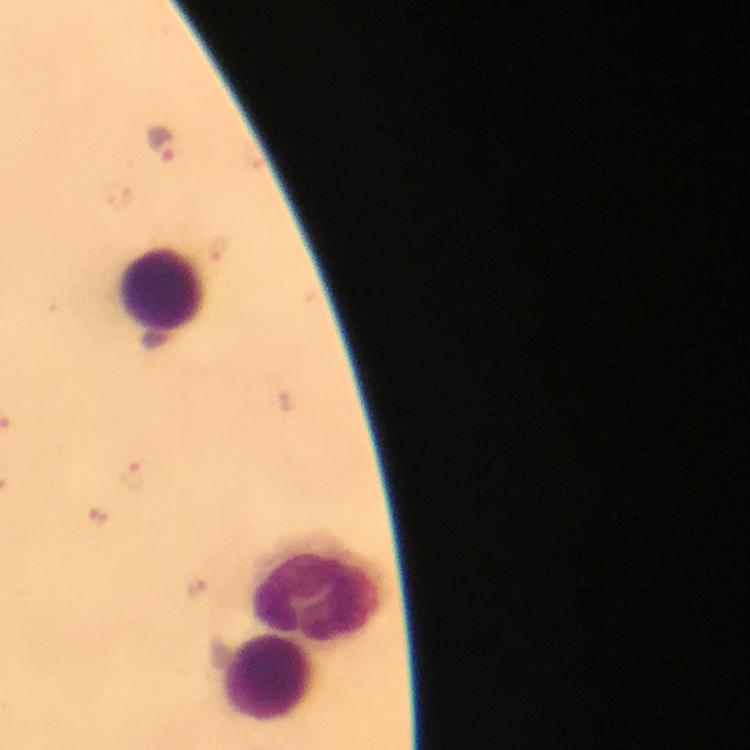 Approximate centers as (x, y) in pixels. Plasmodium parasite locations: (162, 146), (137, 475), (100, 521), (197, 589). Leukocyte locations: (163, 289), (316, 590), (267, 678). Photographed through the microscope with a smartphone camera. At 100x magnification. From a diagnostic examination for malaria. Image is 750×750 pixels. A crop from one field of view. Giemsa-stained preparation. Immersion oil was used. Thick blood smear.